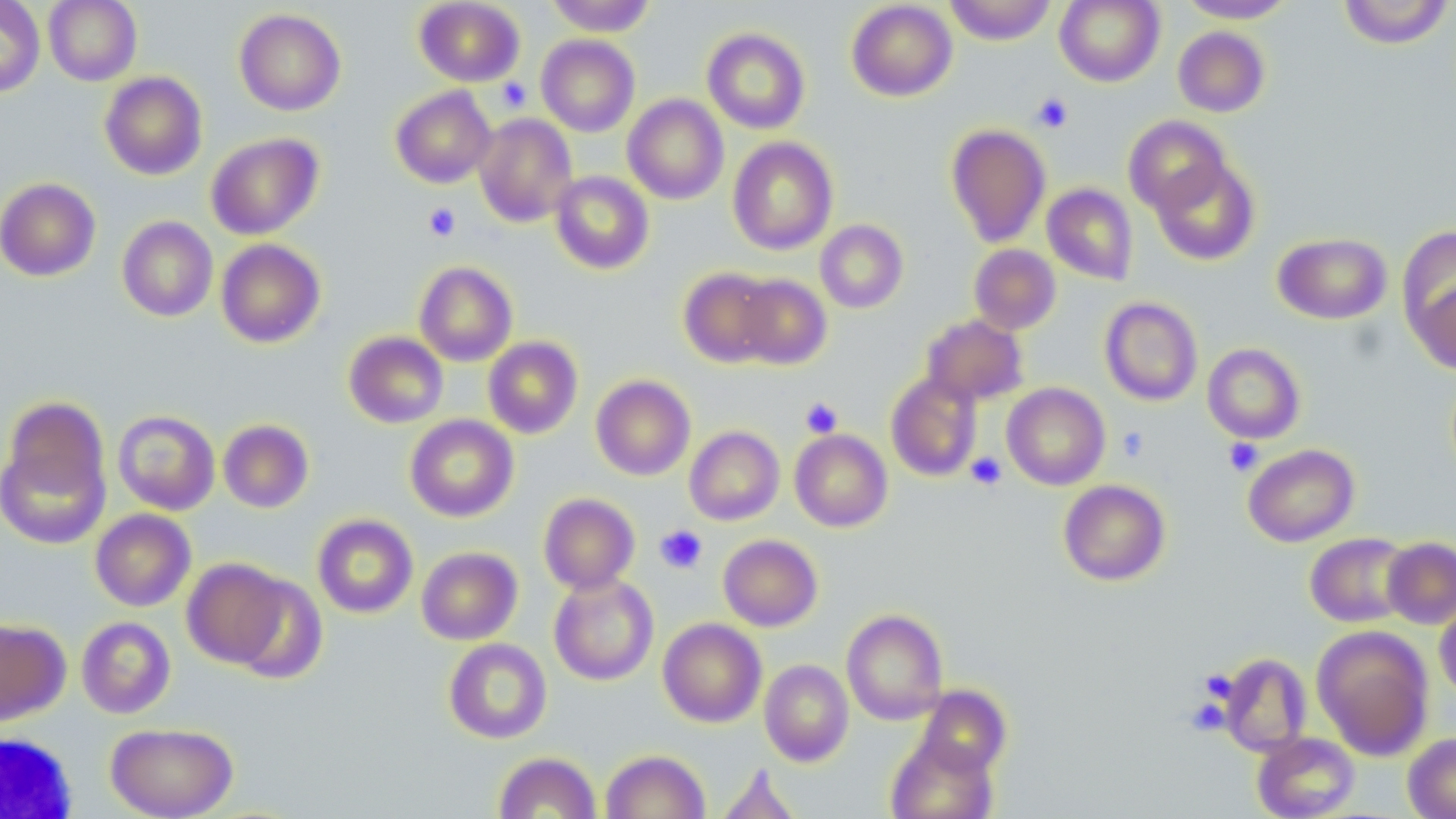
Summary:
  - Coordinate format: approximate bounding boxes as [x1, y1, x2, y2] in pixels
  - Platelet locations: [496, 78, 532, 112], [1032, 93, 1073, 132], [424, 203, 461, 241], [800, 397, 843, 438], [1117, 427, 1149, 462], [1224, 438, 1264, 476], [965, 452, 1007, 490], [655, 524, 707, 574]
  - Uninfected red blood cell locations: [0, 0, 45, 97], [44, 0, 142, 86], [414, 0, 525, 86], [545, 0, 657, 36], [846, 0, 958, 101], [943, 0, 1057, 45], [1055, 0, 1164, 86], [1177, 0, 1297, 23], [1338, 0, 1454, 49], [234, 8, 346, 115], [1173, 26, 1270, 117], [701, 27, 811, 134], [536, 34, 640, 137], [100, 71, 207, 180], [390, 86, 497, 189], [622, 94, 729, 204], [474, 113, 578, 228], [1123, 115, 1231, 215], [946, 123, 1051, 247], [206, 133, 323, 240], [727, 136, 838, 255], [1150, 157, 1259, 266], [550, 171, 654, 274], [0, 177, 101, 281], [1042, 183, 1138, 285], [117, 216, 218, 322], [815, 220, 908, 313], [1398, 226, 1456, 341], [1273, 232, 1392, 324], [215, 239, 325, 348], [969, 244, 1061, 334], [414, 261, 518, 366], [678, 267, 778, 368], [734, 274, 832, 369], [1411, 278, 1456, 375], [1099, 297, 1203, 406], [920, 314, 1028, 406], [344, 331, 448, 428], [483, 336, 583, 438], [1203, 343, 1305, 444], [886, 372, 983, 482], [591, 375, 696, 481], [1002, 383, 1110, 490], [3, 396, 109, 505], [113, 409, 220, 515], [405, 414, 518, 522], [218, 419, 314, 513], [684, 426, 784, 526], [790, 429, 893, 532], [0, 436, 110, 550], [1243, 443, 1359, 547], [1058, 479, 1171, 586], [538, 493, 640, 594], [90, 508, 196, 611], [312, 514, 418, 618], [1305, 532, 1414, 628], [718, 534, 823, 631], [1382, 537, 1456, 629], [416, 546, 522, 645], [182, 558, 290, 669], [548, 572, 659, 686], [228, 574, 328, 684], [1434, 600, 1456, 701], [841, 609, 948, 726], [76, 616, 176, 718], [658, 618, 767, 728], [0, 619, 70, 725], [1312, 625, 1433, 759], [444, 638, 552, 743], [1218, 653, 1312, 757], [759, 659, 853, 766], [913, 684, 1011, 777], [106, 722, 238, 818], [1252, 731, 1360, 819], [1403, 733, 1456, 819], [886, 734, 998, 819], [600, 750, 710, 819], [493, 752, 601, 818], [715, 763, 802, 819]
  - White blood cell locations: [1, 733, 78, 818]
  - Slide-level diagnosis: no evidence of blood parasites
  - Stain: May-Grünwald-Giemsa
  - Preparation: thin blood smear
  - Image size: 1456×819 pixels
  - Magnification: 1000x
  - Modality: optical microscopy
  - Field of view: one of a larger specimen